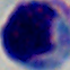

Summary:
  - Magnification: 1000x
  - Identification: white blood cell
  - Modality: micrograph